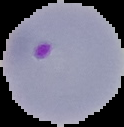
Summary:
  - Result: Plasmodium parasites detected
  - Image type: segmented cell region with the area outside set to black
  - Preparation: thin blood film
  - Image size: 124×127 pixels